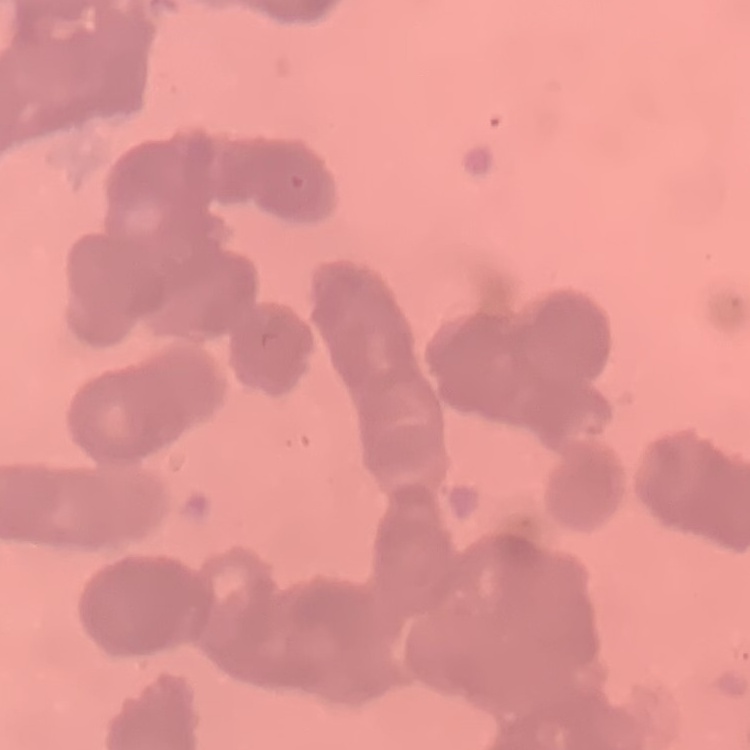

Summary:
  - Red blood cell morphology: rouleaux formation
  - Stain: Field's or Giemsa
  - Image type: one tile cut from a larger photomicrograph
  - Preparation: thin blood film